Report the malaria status of this cell.
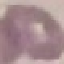

It is uninfected.

Thin blood film. Acquired by smartphone through the microscope eyepiece. Automatically extracted cell patch, resized to 64 × 64 pixels. Giemsa-stained preparation.